Outline each uninfected red blood cell.
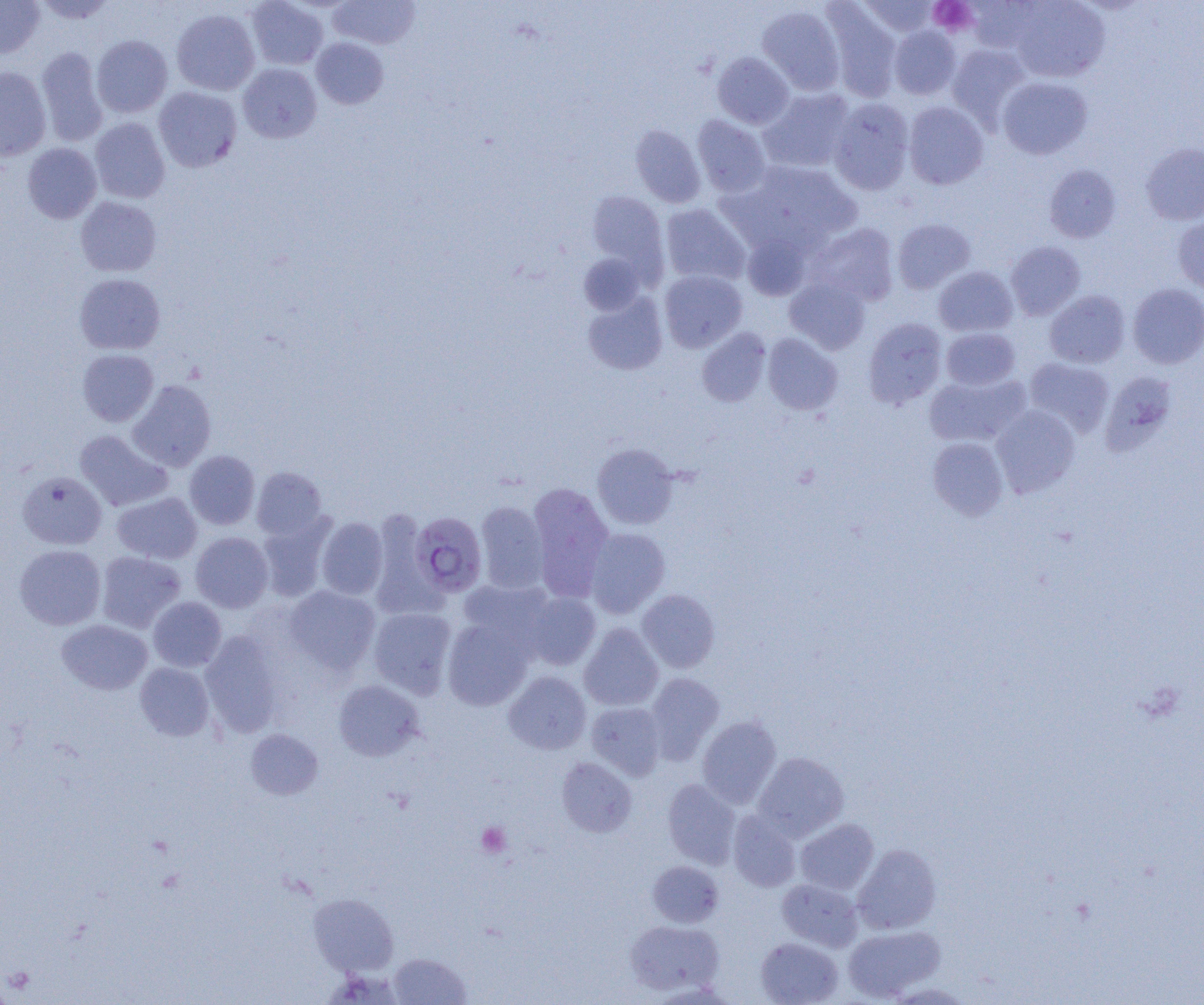
Approximate bounding boxes as (x1,y1)-(x2,y2) corner pairs in pixels.
Uninfected red blood cells: (31,0)-(118,24), (247,0)-(328,70), (329,0)-(420,49), (857,0)-(940,37), (1009,0)-(1110,82), (0,1)-(45,58), (965,1)-(1044,53), (822,3)-(902,102), (757,5)-(845,95), (171,8)-(260,95), (888,26)-(961,100), (91,35)-(172,118), (311,37)-(388,109), (946,44)-(1030,128), (36,46)-(108,147), (712,52)-(794,129), (237,63)-(322,143), (0,67)-(51,160), (997,77)-(1093,159), (154,86)-(242,172), (759,88)-(854,172), (828,98)-(915,195), (903,102)-(989,189), (692,115)-(771,196), (90,117)-(170,204), (630,124)-(706,207), (1140,142)-(1204,225), (23,143)-(101,223), (734,161)-(862,250), (1044,164)-(1121,243), (586,191)-(668,277), (75,196)-(161,277), (660,204)-(750,286), (1173,214)-(1204,294), (892,219)-(975,294), (807,223)-(900,307), (742,232)-(812,300), (1005,241)-(1086,320), (578,253)-(646,315), (934,266)-(1017,337), (659,269)-(747,352), (74,273)-(166,355), (784,277)-(870,354), (1127,283)-(1204,369), (1044,290)-(1131,368), (582,291)-(668,375), (863,318)-(947,409), (696,328)-(771,407), (941,328)-(1021,390), (762,333)-(843,415), (78,349)-(159,426), (1024,357)-(1114,437), (924,372)-(1029,448), (1100,376)-(1169,467), (128,380)-(216,471), (991,405)-(1080,497), (74,430)-(172,511), (928,436)-(1009,519), (592,443)-(679,529), (184,450)-(260,529), (252,467)-(327,540), (18,471)-(107,549), (527,482)-(614,601), (112,491)-(201,563), (475,500)-(549,593), (369,507)-(440,616), (257,515)-(335,601), (316,516)-(388,599), (585,528)-(670,618), (191,532)-(273,613), (15,545)-(106,630), (96,551)-(185,633), (459,579)-(555,651), (285,586)-(380,674), (637,589)-(720,673), (521,591)-(601,670), (148,597)-(226,672), (369,606)-(457,697), (442,617)-(534,710), (56,619)-(152,695), (579,624)-(664,711), (200,630)-(284,737), (135,662)-(214,741), (503,671)-(591,755), (644,672)-(724,762), (332,679)-(425,761), (586,701)-(666,779), (697,716)-(781,808), (246,729)-(322,799), (753,752)-(849,841), (557,757)-(637,837), (662,779)-(741,868), (728,811)-(801,892), (795,818)-(878,895), (853,844)-(941,934), (648,860)-(723,928), (777,878)-(862,951), (309,892)-(398,976), (625,919)-(724,996), (843,925)-(945,1001), (756,937)-(843,1005), (389,953)-(471,1004).

Plasmodium falciparum-infected red blood cell locations: (410,511)-(488,597). Platelet locations: (928,0)-(977,36), (477,822)-(511,857). Slide-level diagnosis: Plasmodium falciparum. Image is 1204×1005 pixels. Light microscopy. Thin blood film. One field of a larger specimen. 1000x magnification.